State the preparation type.
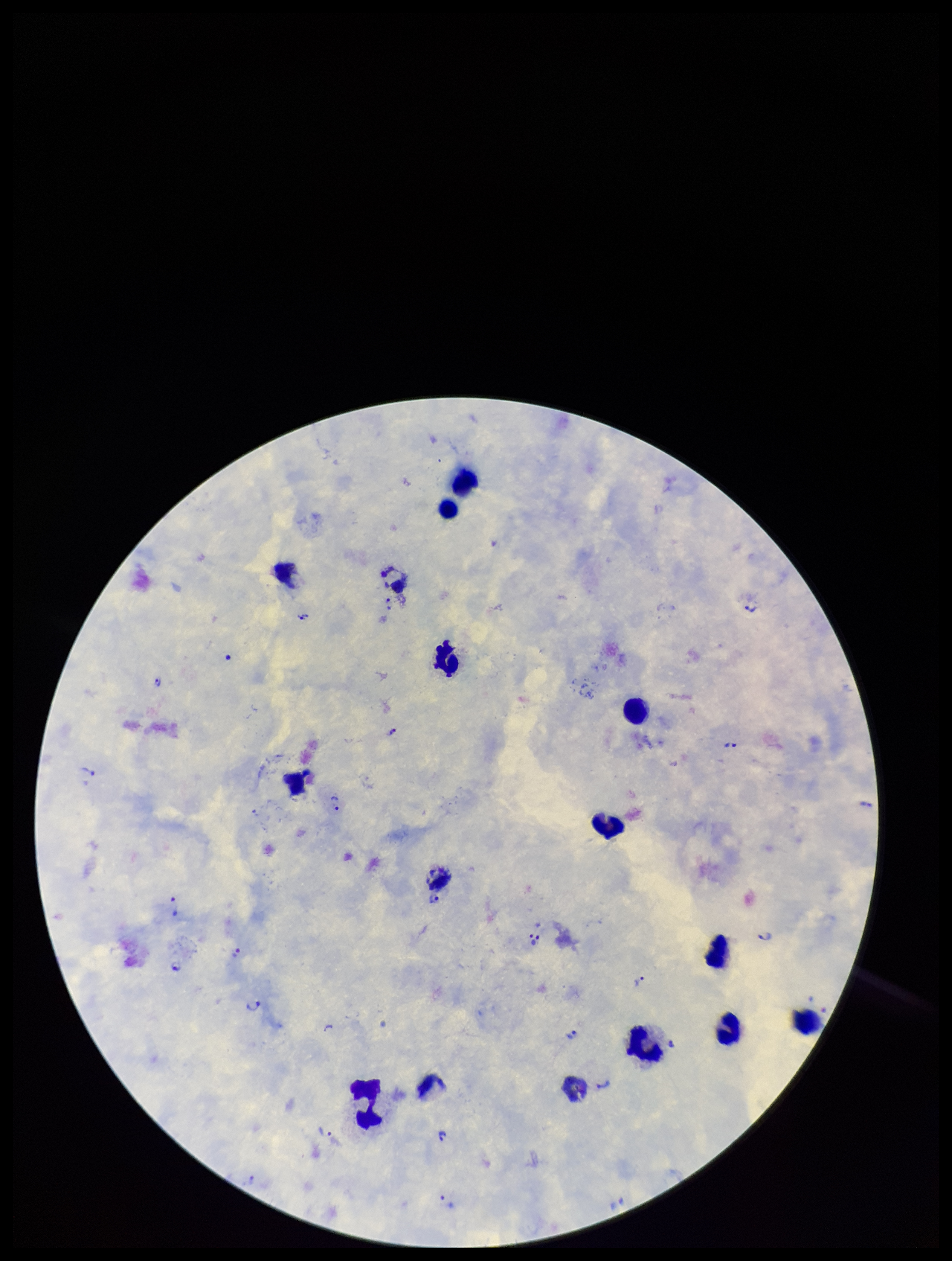
It is a thick blood smear.

{
  "species_reported_for_this_patient": "Plasmodium vivax",
  "leukocyte_count": 14,
  "stain": "Giemsa",
  "image_size": "952×1261 pixels",
  "patient_malaria_status": "positive",
  "plasmodium_parasites": "seen",
  "field_of_view": "single",
  "capture": "smartphone photograph through the microscope eyepiece",
  "parasite_count": 19
}